Assess this cell for malaria.
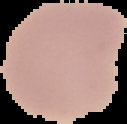
It is uninfected.

image size = 127×124 pixels
image type = segmented cell region on a black background
preparation = thin blood film